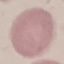
Summary:
  - Result: negative for malaria parasites
  - Capture: smartphone through the microscope eyepiece
  - Image type: automatically extracted cell patch, resized to 64 × 64 pixels
  - Stain: Giemsa
  - Preparation: thin blood smear